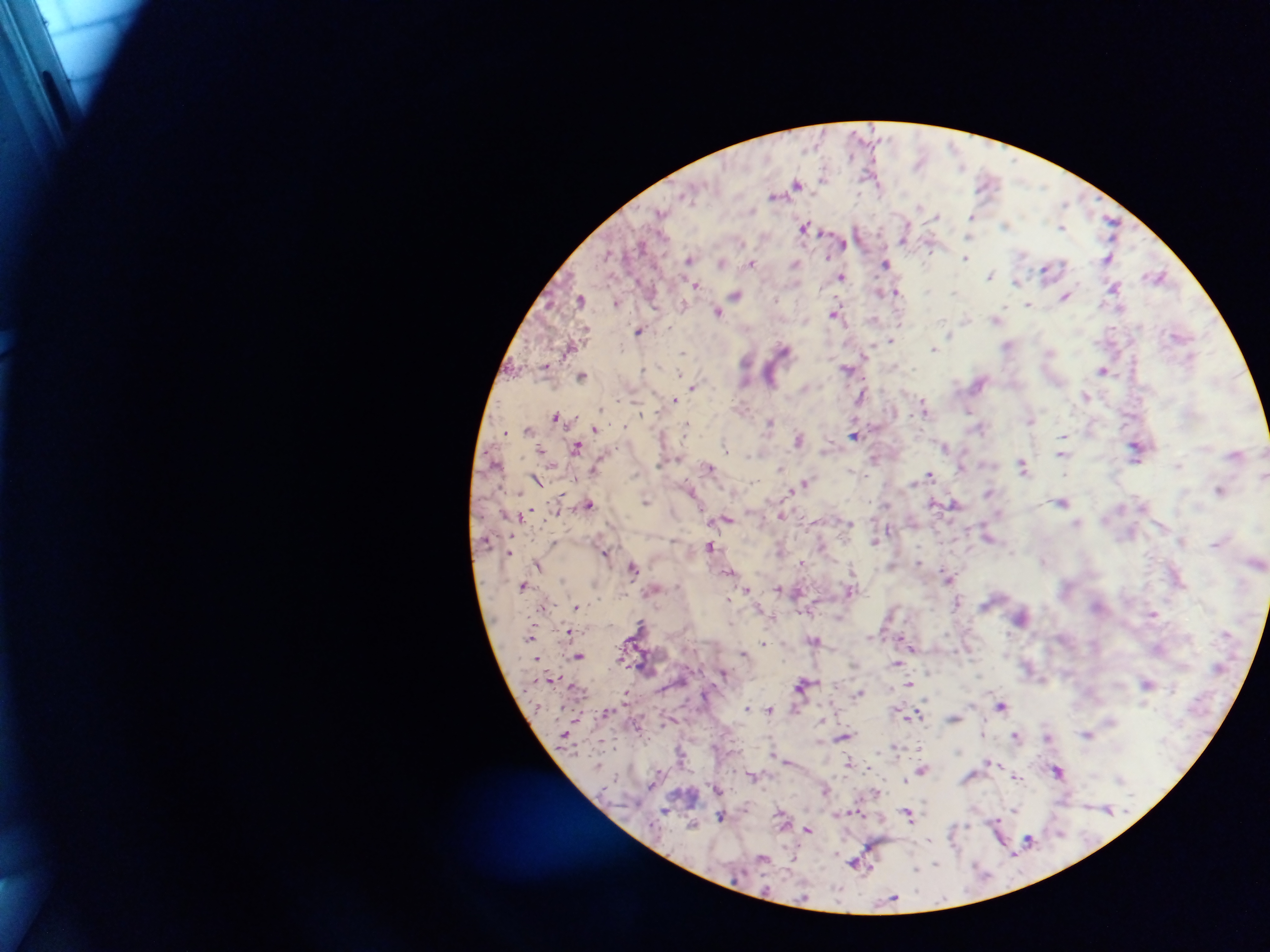
malaria parasite locations = approximate centers as x y in pixels: 920 162; 824 176; 986 182; 796 184; 880 189; 775 194; 1064 202; 920 208; 753 211; 661 213; 936 216; 971 216; 1112 223; 1006 225; 805 227; 1062 228; 969 234; 904 238; 842 243; 930 249; 1022 255; 967 258; 1108 258; 689 259; 722 262; 753 262; 794 264; 886 264; 1045 271; 991 275; 1157 276; 841 277; 1016 282; 695 285; 1114 288; 928 291; 879 292; 897 292; 953 293; 737 295; 1065 297; 580 299; 777 299; 617 303; 683 304; 1028 305; 717 312; 835 313; 996 319; 965 320; 640 330; 585 331; 949 333; 1179 336; 890 340; 1008 345; 934 349; 784 350; 1049 351; 683 352; 868 352; 745 361; 546 365; 848 368; 644 369; 1104 370; 681 374; 582 376; 979 382; 692 387; 1086 396; 675 400; 925 408; 969 410; 556 416; 1031 420; 770 422; 687 425; 624 426; 981 428; 595 429; 528 430; 506 432; 854 434; 1063 437; 798 439; 945 446; 577 447; 725 447; 1136 447; 541 449; 1062 454; 749 455; 874 459; 1023 465; 709 467; 961 467; 594 468; 780 469; 1065 473; 929 475; 1265 475; 538 481; 805 483; 1221 491; 988 492; 647 501; 1061 502; 589 503; 934 504; 954 505; 782 515; 727 519; 850 523; 1077 523; 889 529; 987 536; 875 541; 1182 541; 554 543; 711 546; 605 553; 919 561; 1043 561; 801 563; 538 565; 633 568; 852 570; 730 572; 949 577; 523 585; 778 588; 850 589; 747 590; 729 599; 957 602; 577 607; 1153 614; 839 617; 641 624; 569 631; 530 636; 871 637; 815 640; 904 642; 763 643; 743 653; 579 656; 896 664; 1147 683; 802 684; 910 684; 858 694; 1001 706; 747 708; 770 711; 918 715; 953 718; 821 719; 983 733; 1088 734; 1015 735; 844 737; 1047 737; 896 747; 919 748; 849 762; 922 770; 1057 770; 1016 776; 753 777; 905 779; 1120 779; 825 790; 1107 809; 1014 810; 908 814; 721 816; 996 821; 692 825; 808 830; 1028 839; 868 847; 762 858; 855 863; 935 864; 867 867; 916 868; 892 899
country = Ghana
preparation = thick blood film
field of view = single
image size = 1270×952 pixels
capture = mobile-phone photograph through a microscope